State which parasite is depicted.
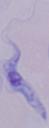
A trypanosome.

Summary:
  - Modality: micrograph
  - Magnification: 1000x